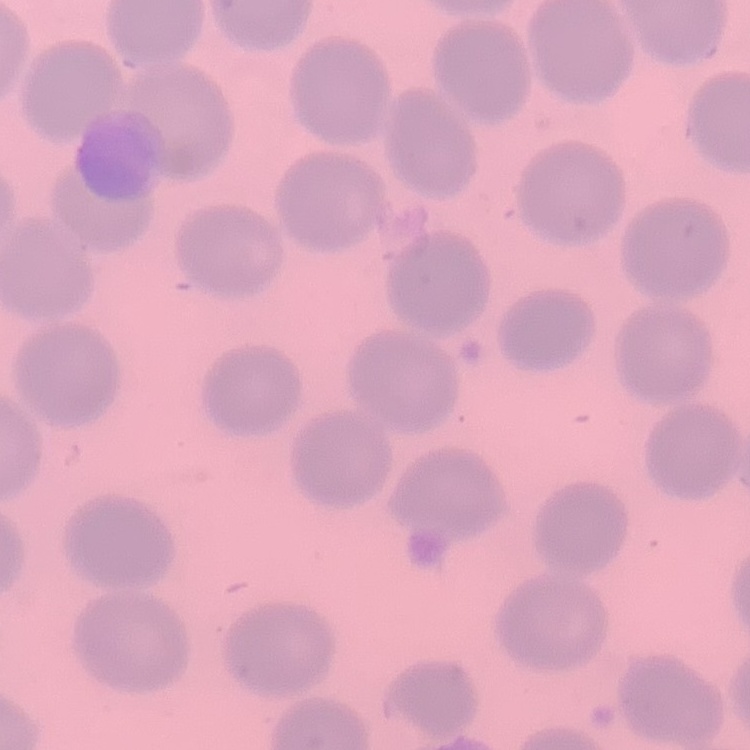

{
  "erythrocyte_morphology": "no rouleaux formation",
  "stain": "Field's or Giemsa",
  "image_type": "one tile cut from a larger photomicrograph",
  "preparation": "thin blood smear"
}